Identify the parasite.
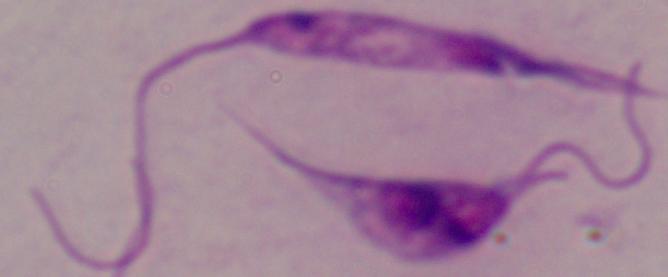
This is Leishmania.

modality = micrograph
magnification = 1000x